Classify this cell by malaria status.
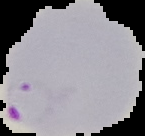
Parasitized.

From a thin blood film. Image is 145×136 pixels. Segmented cell region on a black background.